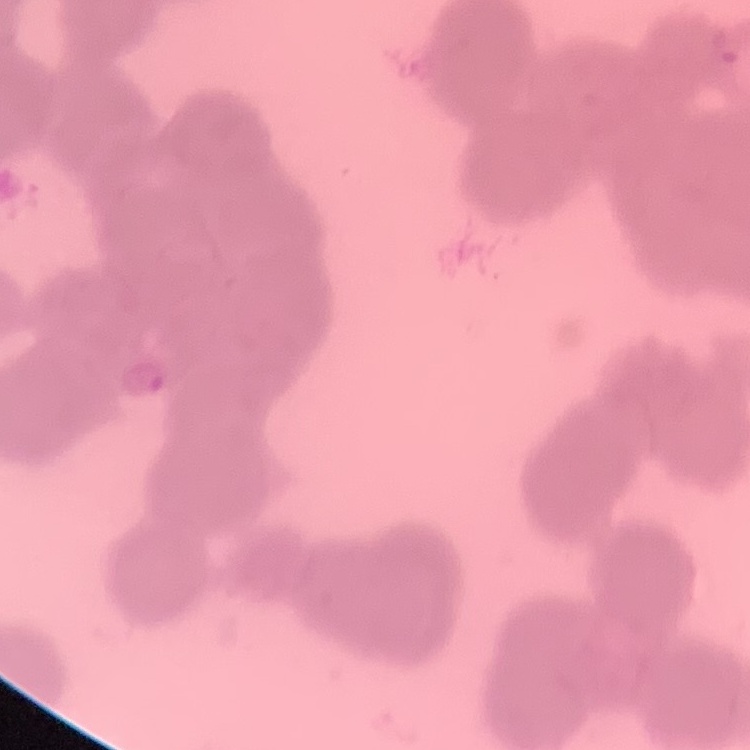

The red blood cells show rouleaux formation. Stained with either Field's or Giemsa. Thin peripheral smear. One tile cut from a larger photomicrograph.